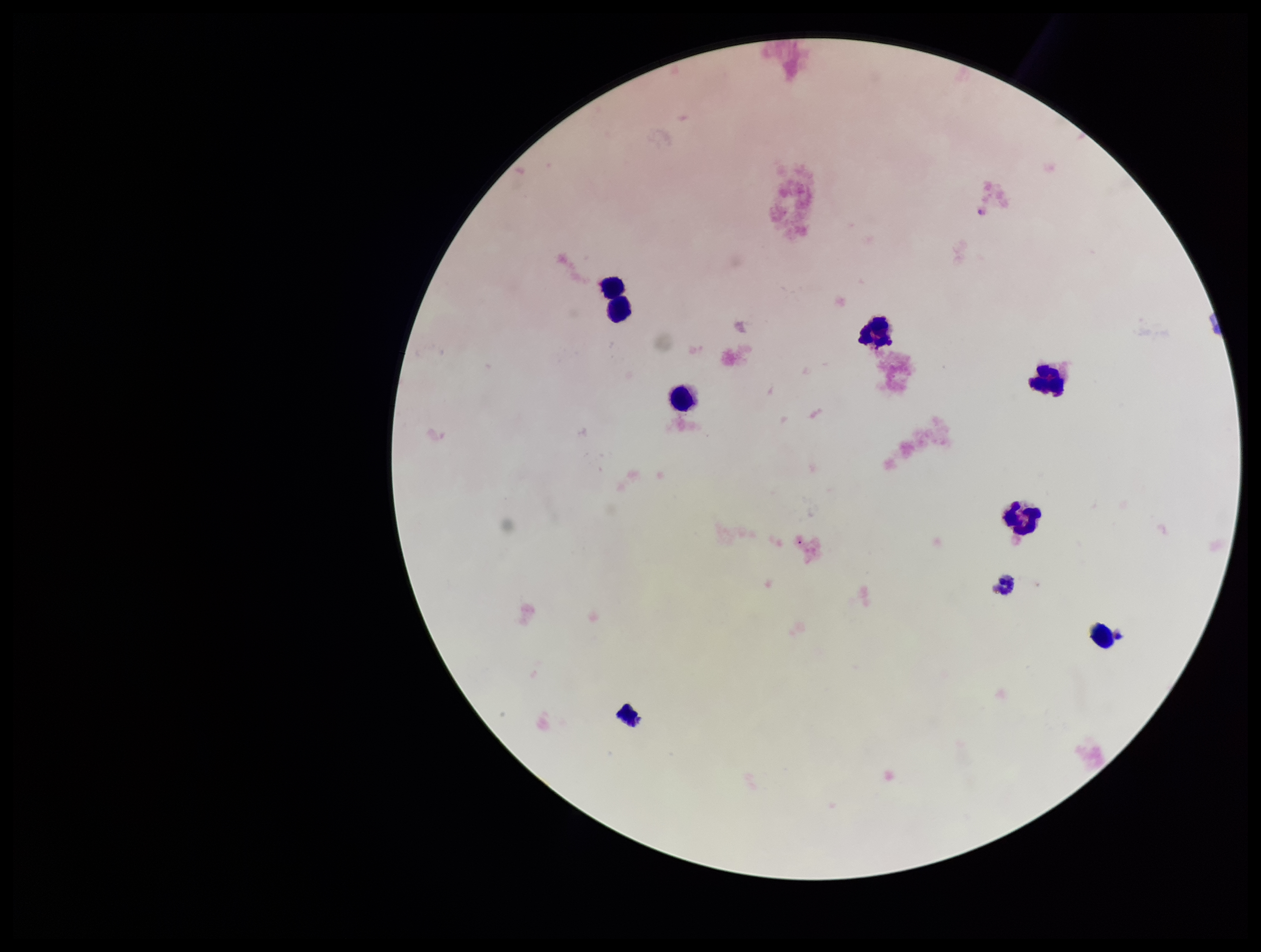
Leukocyte count: 8. Plasmodium parasites: none identified. Photographed through the microscope eyepiece with a smartphone camera. Parasite count: 0. Image is 1261×952 pixels. Preparation: thick blood smear. Giemsa stain. Single field of view. Patient malaria status: negative.